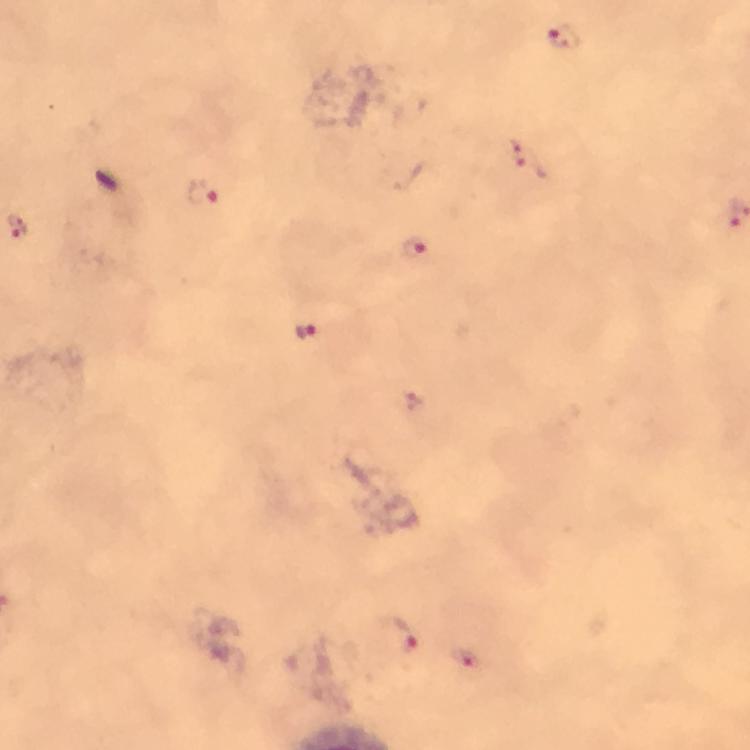 Approximate centers as [x, y] in pixels. Plasmodium parasite locations: [565, 37], [529, 159], [201, 191], [16, 226], [413, 247], [306, 333], [399, 637], [463, 659]. From a malaria diagnostic workup. Cropped region of a single field of view. Immersion oil applied. Photographed through the microscope with a smartphone camera. Giemsa stain. At 100x magnification. Image is 750×750 pixels. Thick smear.